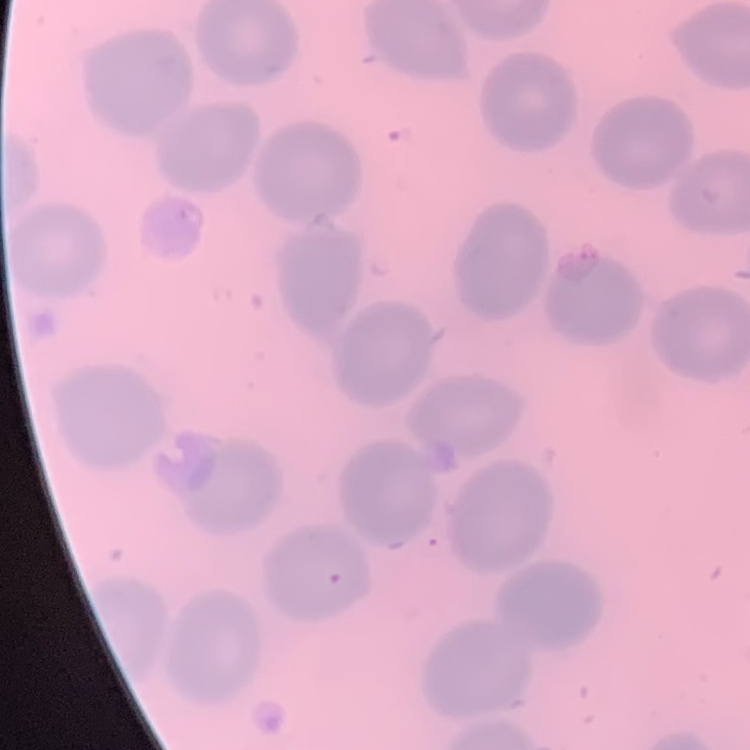
The red blood cells exhibit no rouleaux formation. Square crop of a larger photomicrograph. Stained with either Field's or Giemsa. Thin blood film.